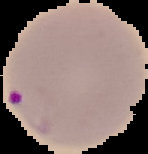 Result: Plasmodium parasites detected. From a thin blood film. Image is 148×154 pixels. The area outside the segmented cell region is set to black.